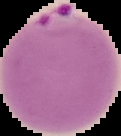

result = malaria parasites detected
image size = 121×136 pixels
preparation = thin blood smear
image type = segmented cell region on a black background